Comment on the morphology of the red blood cells.
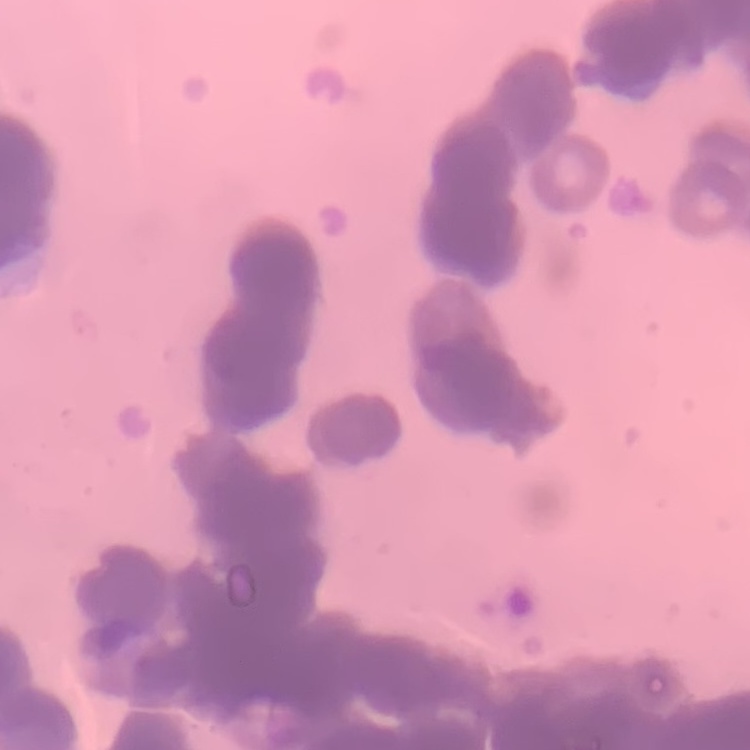

Rouleaux formation.

One tile cut from a larger photomicrograph. Stained with either Field's or Giemsa. Thin blood smear.